Point out each leukocyte.
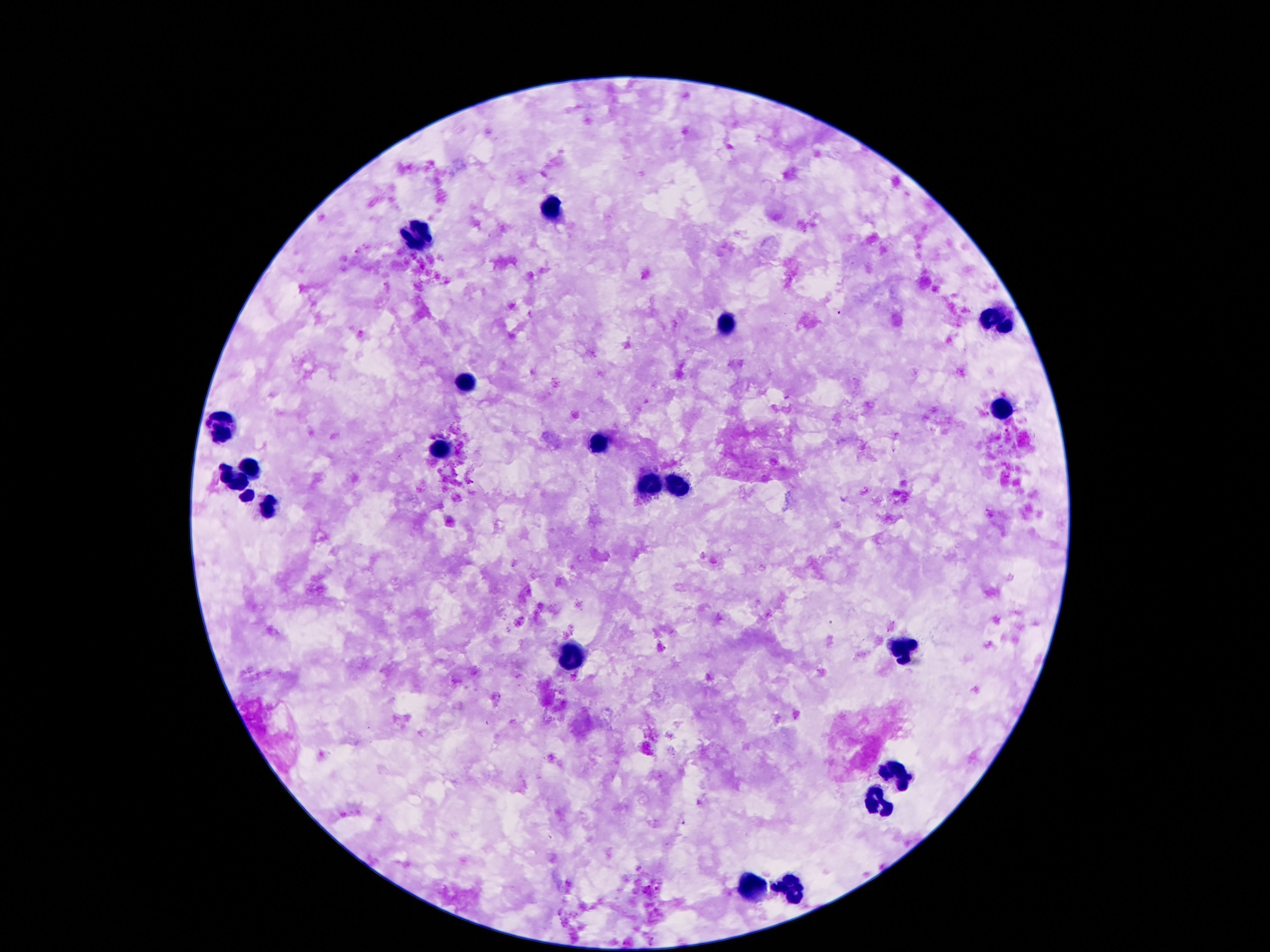

Approximate centers as (x, y) in pixels.
Leukocytes: (550, 210), (417, 234), (998, 320), (723, 329), (464, 386), (998, 413), (221, 428), (597, 448), (440, 451), (253, 467), (233, 480), (678, 484), (650, 490), (246, 496), (267, 508), (907, 647), (569, 654), (899, 773), (876, 802), (750, 890), (794, 890).

Giemsa-stained preparation. Image is 1270×952 pixels. 100x magnification. Patient malaria status: not infected. Thick blood film. One field from this slide. Smartphone photograph taken through the microscope eyepiece.